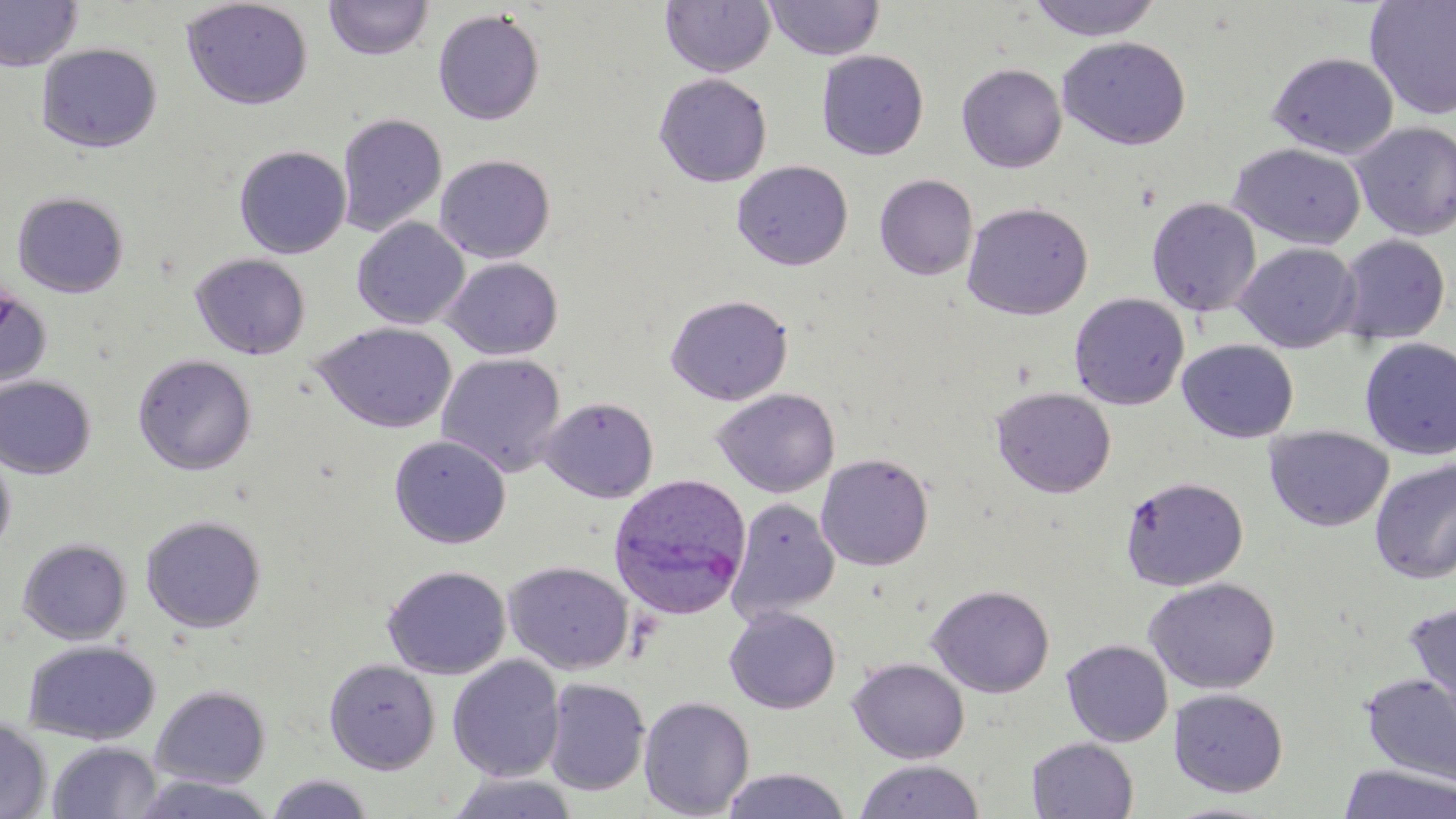
Summary:
  - Coordinate format: approximate bounding boxes as [x1, y1, x2, y2] in pixels
  - Plasmodium ovale-infected red blood cell locations: [608, 473, 752, 619]
  - Uninfected red blood cell locations: [0, 0, 83, 72], [181, 0, 313, 110], [324, 0, 434, 61], [659, 0, 776, 77], [765, 0, 884, 60], [1026, 0, 1163, 41], [1364, 1, 1456, 120], [432, 9, 545, 125], [1058, 36, 1192, 150], [36, 42, 162, 153], [816, 50, 929, 161], [1266, 51, 1400, 159], [956, 63, 1067, 173], [654, 73, 773, 187], [336, 113, 448, 237], [1352, 121, 1456, 241], [1228, 142, 1366, 249], [234, 145, 351, 259], [435, 154, 555, 263], [731, 160, 853, 271], [874, 174, 978, 281], [875, 185, 1076, 300], [12, 191, 129, 297], [1146, 198, 1262, 317], [961, 201, 1093, 321], [352, 217, 470, 329], [1336, 234, 1451, 345], [1234, 242, 1361, 352], [190, 253, 310, 359], [443, 257, 563, 360], [0, 283, 53, 394], [1069, 292, 1190, 410], [665, 294, 793, 406], [313, 322, 457, 434], [1359, 337, 1456, 460], [1177, 339, 1300, 443], [133, 353, 257, 475], [436, 353, 566, 477], [0, 375, 97, 479], [991, 386, 1116, 498], [712, 388, 840, 498], [539, 396, 659, 503], [1263, 426, 1394, 532], [389, 434, 512, 548], [0, 444, 16, 560], [816, 453, 934, 571], [1369, 459, 1456, 584], [1120, 475, 1248, 591], [727, 497, 840, 622], [141, 515, 266, 633], [18, 537, 132, 645], [503, 560, 634, 675], [383, 565, 511, 679], [1144, 577, 1281, 694], [926, 584, 1055, 698], [1403, 603, 1456, 727], [724, 606, 841, 714], [22, 639, 161, 744], [1061, 639, 1173, 746], [447, 656, 565, 782], [848, 657, 970, 764], [324, 658, 440, 774], [1360, 672, 1456, 787], [542, 678, 650, 796], [151, 684, 271, 788], [1169, 688, 1288, 797], [638, 696, 755, 818], [0, 718, 51, 819], [1026, 738, 1138, 818], [48, 740, 162, 819], [854, 760, 984, 818], [1338, 763, 1456, 819], [719, 767, 853, 819], [265, 773, 374, 818], [445, 773, 580, 818], [129, 774, 278, 818], [1163, 800, 1286, 818]
  - Slide-level diagnosis: Plasmodium ovale
  - Image size: 1456×819 pixels
  - Field of view: one of a larger specimen
  - Modality: optical microscopy
  - Magnification: 1000x
  - Preparation: thin blood film
  - Stain: May-Grünwald-Giemsa